State which parasite is depicted.
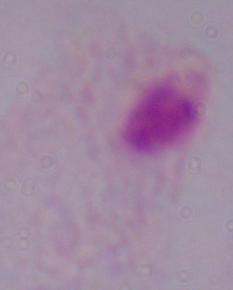

A trichomonad.

Summary:
  - Modality: micrograph
  - Magnification: 1000x